Give a bounding box for every artifact (stain precipitate or debris).
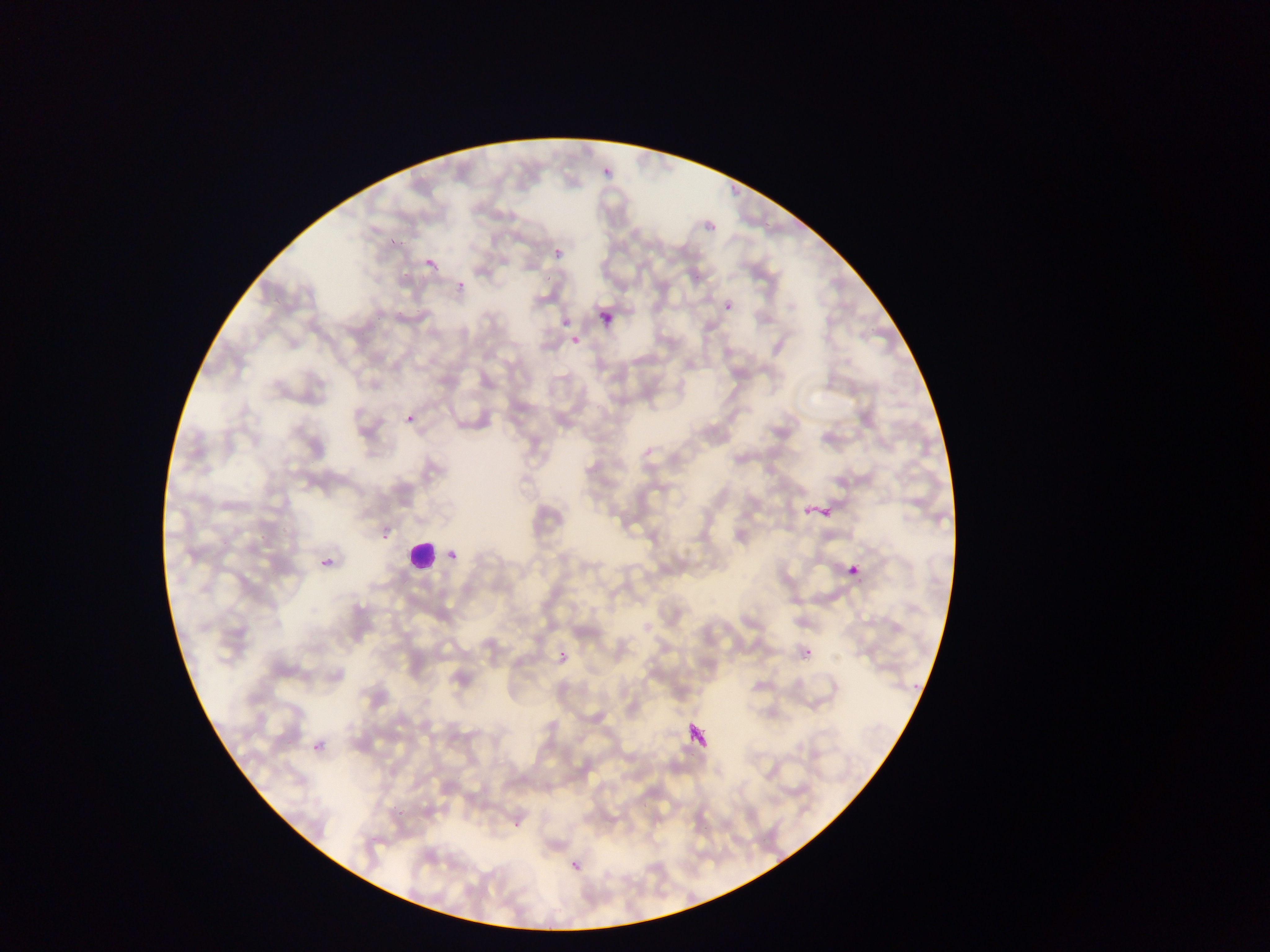

Approximate bounding boxes as [left, top, right, bottom] in pixels.
Artifacts (stain precipitate or debris): [803, 500, 832, 520], [845, 563, 861, 576], [688, 718, 710, 748].

capture = mobile-phone photograph through a microscope
field of view = single
preparation = thin blood smear
country = Ghana
image size = 1270×952 pixels
Plasmodium parasite locations = approximate bounding boxes as [left, top, right, bottom] in pixels: [603, 164, 612, 175], [706, 223, 716, 230], [390, 234, 395, 245], [554, 249, 565, 259], [426, 257, 434, 268], [431, 266, 441, 272], [694, 268, 702, 281], [458, 280, 466, 288], [725, 301, 732, 314], [561, 320, 569, 328], [568, 334, 582, 345], [408, 411, 415, 423], [383, 534, 391, 542], [445, 546, 458, 558], [319, 560, 327, 569], [559, 648, 566, 660], [806, 648, 812, 658], [912, 682, 918, 690], [310, 740, 320, 752], [689, 751, 697, 758], [639, 801, 648, 809], [513, 822, 521, 827], [705, 824, 709, 832], [575, 866, 584, 872] | approximate [x, y] pixel centers of objects too small to bound: [549, 278], [400, 814], [574, 864]
leukocyte locations = approximate bounding boxes as [left, top, right, bottom] in pixels: [596, 310, 615, 326], [409, 532, 437, 570]